Mark where platelets are.
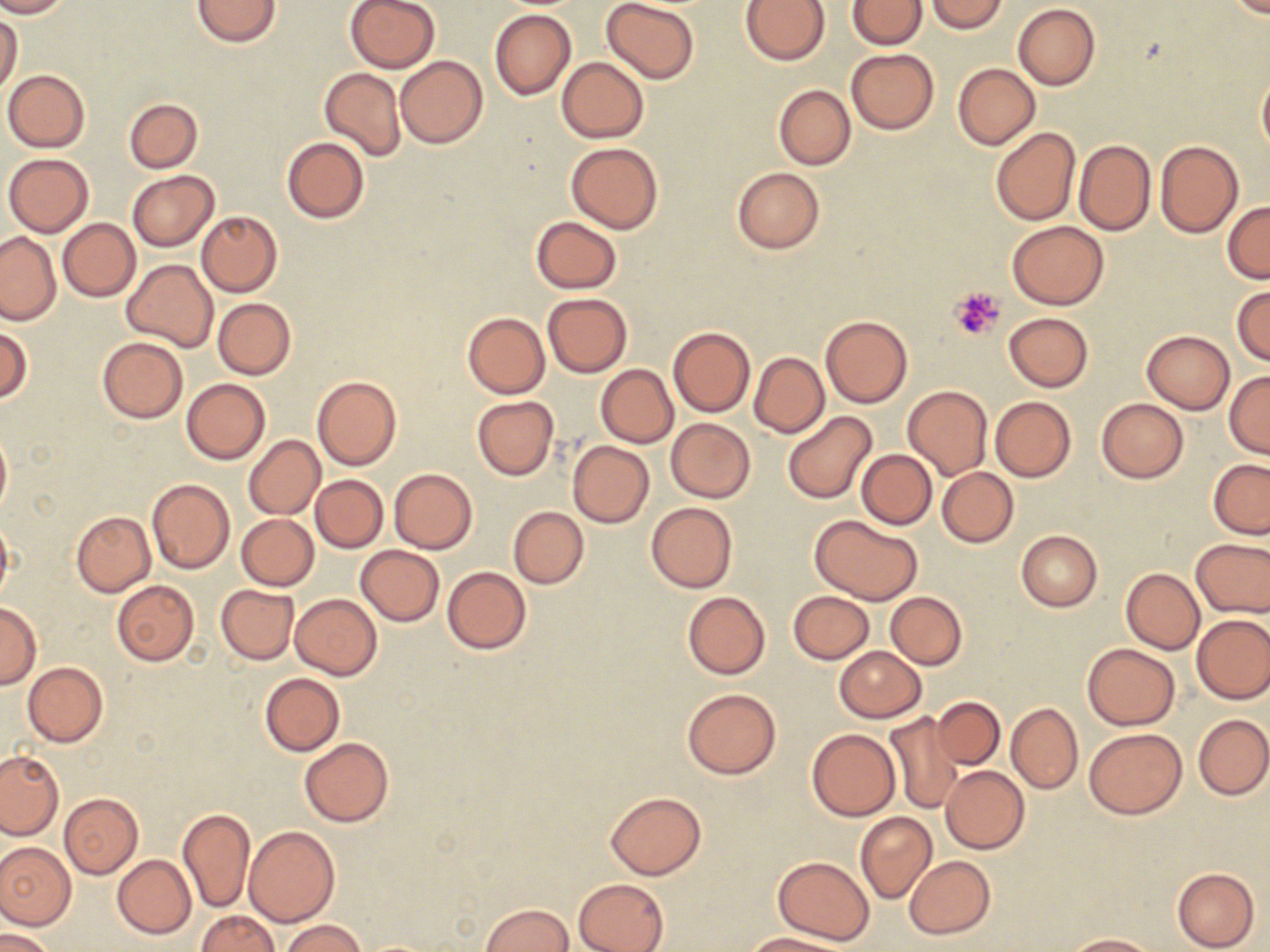
Approximate bounding boxes as (x1, y1, x2, y2) in pixels.
Platelets: (951, 287, 1005, 341).

Uninfected red blood cell locations: (0, 0, 75, 18), (192, 0, 281, 46), (344, 0, 440, 73), (601, 0, 701, 84), (847, 0, 927, 50), (926, 0, 1007, 34), (1219, 0, 1270, 17), (740, 1, 831, 66), (1012, 3, 1100, 90), (489, 9, 576, 100), (0, 11, 23, 97), (847, 48, 939, 134), (395, 55, 488, 148), (556, 56, 649, 143), (952, 63, 1040, 149), (319, 66, 405, 162), (2, 69, 90, 152), (1257, 69, 1270, 156), (773, 84, 856, 169), (123, 97, 203, 173), (990, 127, 1080, 227), (282, 136, 370, 223), (1074, 139, 1155, 235), (1154, 140, 1243, 238), (565, 143, 663, 233), (3, 152, 93, 236), (731, 168, 825, 254), (126, 170, 219, 251), (1223, 201, 1270, 283), (197, 211, 282, 296), (531, 216, 622, 293), (58, 218, 140, 301), (1007, 221, 1109, 309), (0, 231, 60, 324), (122, 260, 217, 352), (1231, 284, 1270, 366), (543, 293, 632, 376), (213, 297, 296, 379), (462, 310, 551, 399), (1005, 312, 1092, 392), (820, 315, 913, 407), (0, 325, 32, 405), (668, 326, 754, 417), (1140, 330, 1234, 414), (98, 337, 187, 423), (749, 351, 829, 437), (597, 364, 678, 447), (1224, 371, 1270, 457), (311, 375, 401, 471), (181, 377, 271, 465), (903, 386, 993, 480), (471, 396, 559, 480), (990, 396, 1077, 482), (1096, 398, 1188, 483), (782, 410, 877, 504), (665, 418, 755, 502), (0, 429, 11, 519), (245, 436, 324, 519), (567, 440, 654, 528), (856, 449, 937, 529), (1208, 459, 1270, 539), (938, 466, 1019, 547), (389, 468, 478, 554), (310, 474, 388, 553), (147, 478, 234, 574), (646, 501, 737, 592), (508, 506, 589, 588), (72, 511, 155, 596), (0, 513, 13, 605), (811, 514, 923, 606), (237, 515, 319, 590), (229, 516, 308, 663), (1016, 530, 1102, 611), (1192, 537, 1270, 618), (356, 545, 444, 626), (441, 566, 531, 654), (1121, 568, 1205, 653), (111, 580, 200, 666), (216, 583, 298, 664), (787, 590, 874, 663), (683, 591, 770, 679), (884, 591, 967, 669), (290, 593, 382, 679), (0, 602, 42, 688), (1192, 614, 1270, 703), (1082, 643, 1180, 730), (835, 646, 926, 721), (23, 661, 108, 747), (260, 673, 345, 755), (682, 688, 781, 779), (932, 696, 1005, 770), (1006, 703, 1082, 793), (887, 710, 964, 813), (1194, 714, 1270, 800), (806, 728, 901, 821), (1084, 728, 1187, 818), (299, 738, 393, 827), (0, 750, 62, 839), (940, 766, 1029, 853), (605, 791, 707, 880), (59, 793, 143, 878), (178, 810, 256, 913), (855, 812, 937, 903), (244, 826, 339, 927), (869, 826, 983, 924), (0, 843, 76, 929), (112, 854, 196, 938), (904, 855, 995, 940), (772, 856, 875, 946), (1170, 866, 1260, 951), (574, 878, 669, 952), (480, 903, 574, 952), (195, 910, 280, 951), (278, 919, 367, 952), (1, 929, 55, 952), (744, 932, 844, 951), (1064, 933, 1156, 951). Slide-level diagnosis: no evidence of blood parasites. Light microscopy. One field of a larger specimen. Captured at 1000x magnification. Image is 1270×952 pixels. Thin blood film. May-Grünwald-Giemsa stain.